Report the malaria status of this cell.
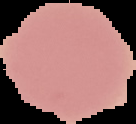
Uninfected.

Summary:
  - Image size: 136×124 pixels
  - Image type: segmented cell region on a black background
  - Preparation: thin blood smear